Give the extent of all uninfected red blood cells.
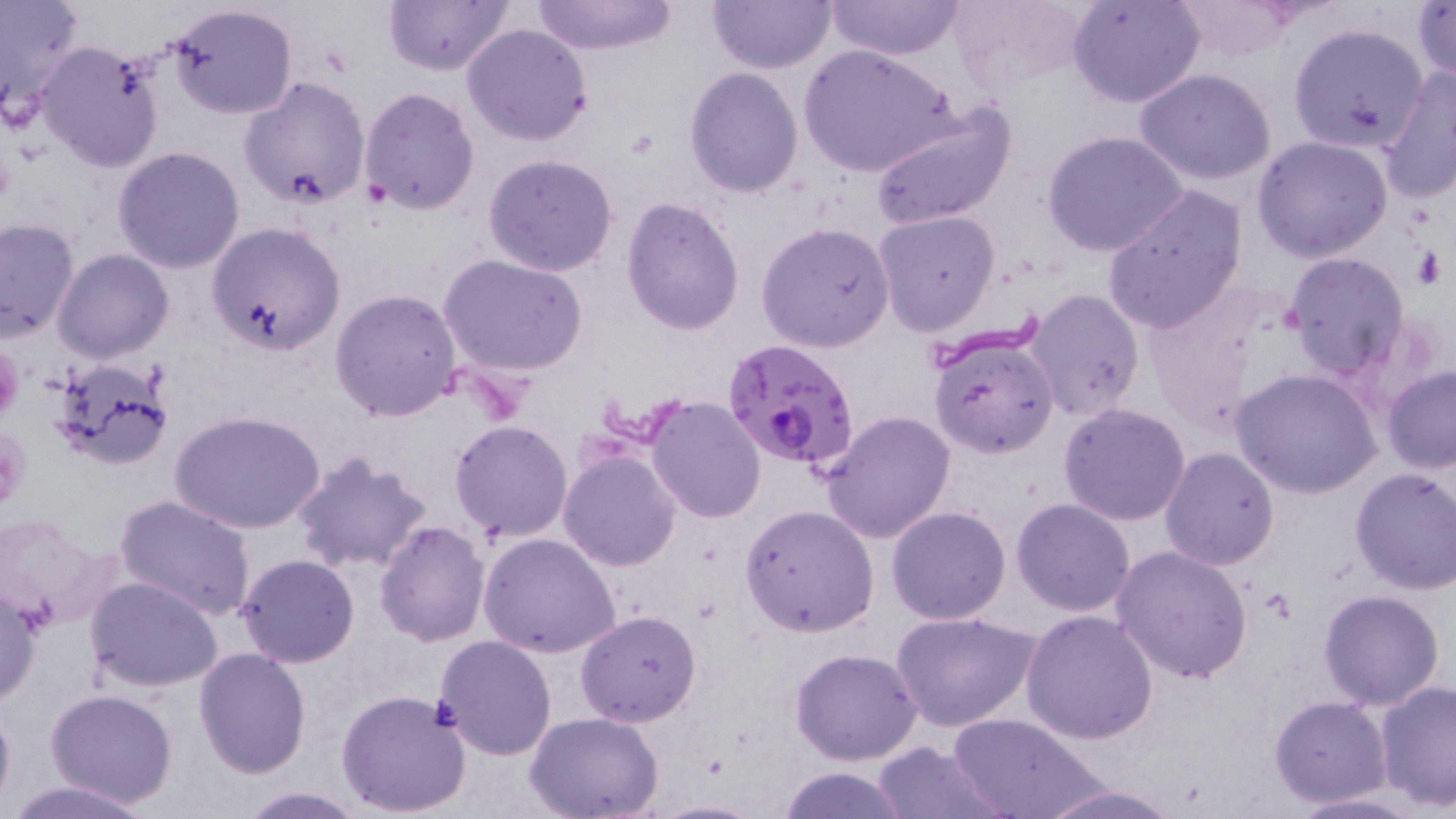
Approximate bounding boxes as [x1, y1, x2, y2] in pixels.
Uninfected red blood cells: [531, 0, 681, 55], [707, 0, 837, 74], [828, 0, 966, 61], [947, 0, 1092, 98], [1068, 0, 1206, 108], [1164, 0, 1308, 63], [0, 1, 87, 125], [382, 1, 515, 76], [1412, 2, 1456, 84], [165, 3, 298, 120], [462, 22, 593, 146], [1287, 22, 1429, 155], [36, 41, 168, 173], [801, 45, 959, 178], [1377, 65, 1456, 205], [683, 67, 805, 197], [1135, 68, 1279, 185], [238, 76, 371, 211], [358, 88, 481, 215], [869, 100, 1018, 230], [1042, 130, 1189, 257], [1252, 135, 1395, 263], [112, 147, 247, 274], [482, 154, 620, 278], [1102, 186, 1249, 334], [621, 197, 745, 336], [874, 210, 998, 335], [0, 217, 80, 341], [206, 221, 348, 355], [756, 223, 896, 352], [52, 248, 176, 364], [1281, 251, 1412, 381], [438, 253, 590, 378], [1138, 286, 1276, 434], [330, 287, 462, 422], [1026, 288, 1145, 421], [928, 335, 1059, 458], [49, 357, 174, 472], [1381, 365, 1456, 472], [1233, 368, 1382, 500], [644, 395, 766, 522], [1058, 403, 1191, 525], [820, 410, 955, 543], [171, 411, 326, 536], [449, 419, 574, 543], [1159, 446, 1281, 570], [288, 449, 434, 574], [559, 449, 681, 572], [1350, 467, 1456, 595], [113, 493, 260, 622], [1012, 498, 1136, 616], [739, 504, 879, 636], [886, 506, 1012, 625], [0, 508, 122, 630], [373, 519, 490, 647], [478, 533, 622, 660], [1113, 546, 1253, 684], [236, 553, 360, 668], [84, 574, 225, 693], [0, 584, 43, 708], [1318, 588, 1445, 710], [1021, 608, 1158, 743], [576, 610, 702, 726], [892, 612, 1038, 732], [433, 634, 557, 760], [191, 647, 311, 777], [791, 647, 923, 765], [1374, 679, 1455, 812], [336, 688, 474, 817], [45, 689, 179, 808], [1270, 696, 1393, 807], [0, 698, 15, 813], [949, 712, 1102, 819], [527, 713, 663, 819], [870, 741, 1007, 818], [776, 764, 911, 819], [2, 778, 163, 818], [1035, 783, 1185, 818], [235, 786, 370, 818], [1287, 793, 1429, 818].

Platelet locations: [0, 345, 23, 425], [0, 429, 31, 508]. Plasmodium falciparum-infected red blood cell locations: [721, 338, 861, 475]. Slide-level diagnosis: Plasmodium falciparum. Captured at 1000x magnification. Light microscopy. Image is 1456×819 pixels. May-Grünwald-Giemsa-stained preparation. Thin blood film. Single field of view.